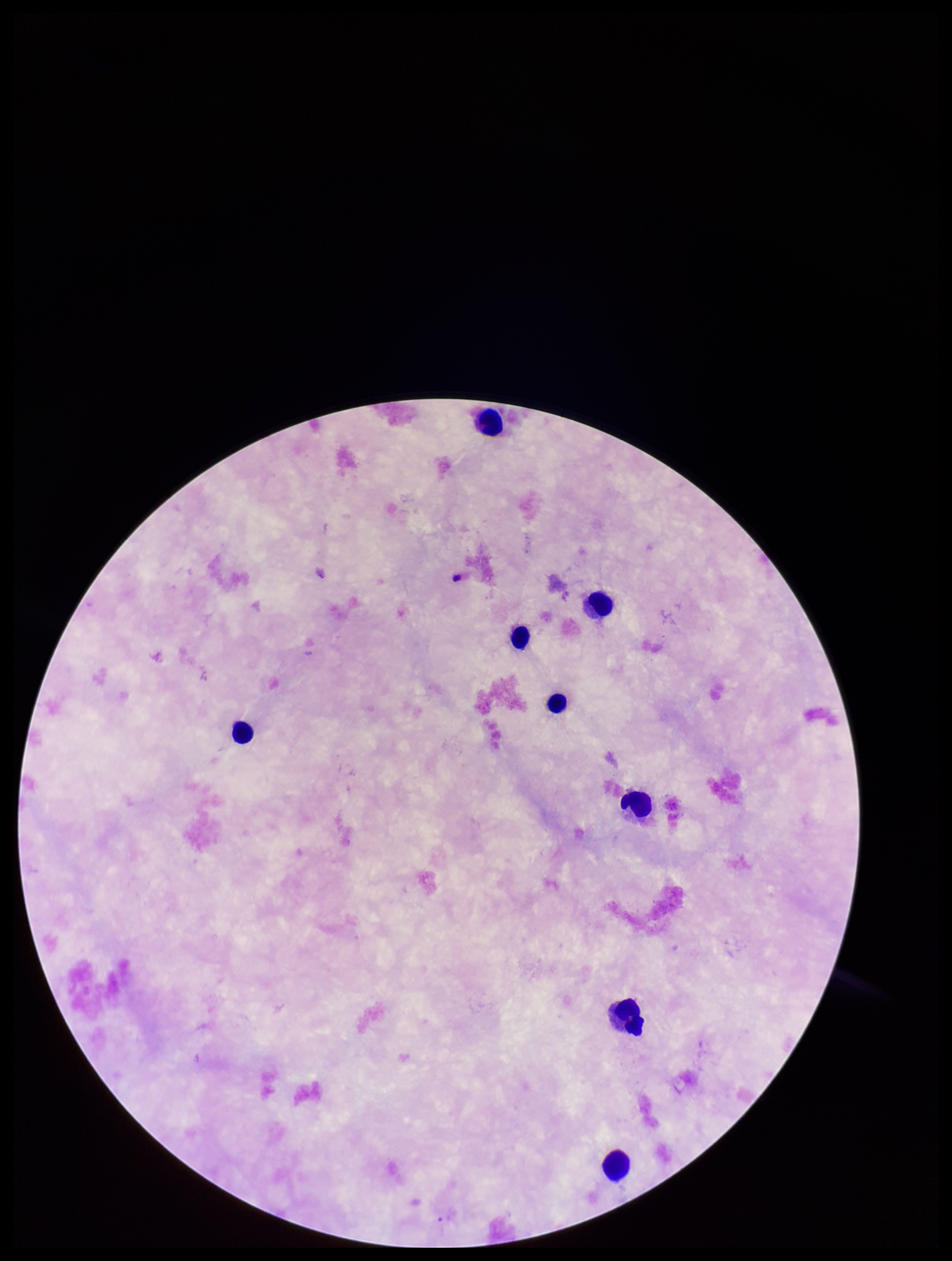
patient malaria status = negative
stain = Giemsa
preparation = thick
field of view = one from this slide
Plasmodium parasites = none identified
parasite count = 0
capture = smartphone photograph through the microscope eyepiece
leukocyte count = 8
image size = 952×1261 pixels